Report the malaria status of this cell.
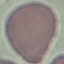

Uninfected.

Thin smear of blood. Acquired by smartphone through the microscope eyepiece. Giemsa stain. Cell patch, automatically extracted from a larger field of view and resized to 64 × 64 pixels.